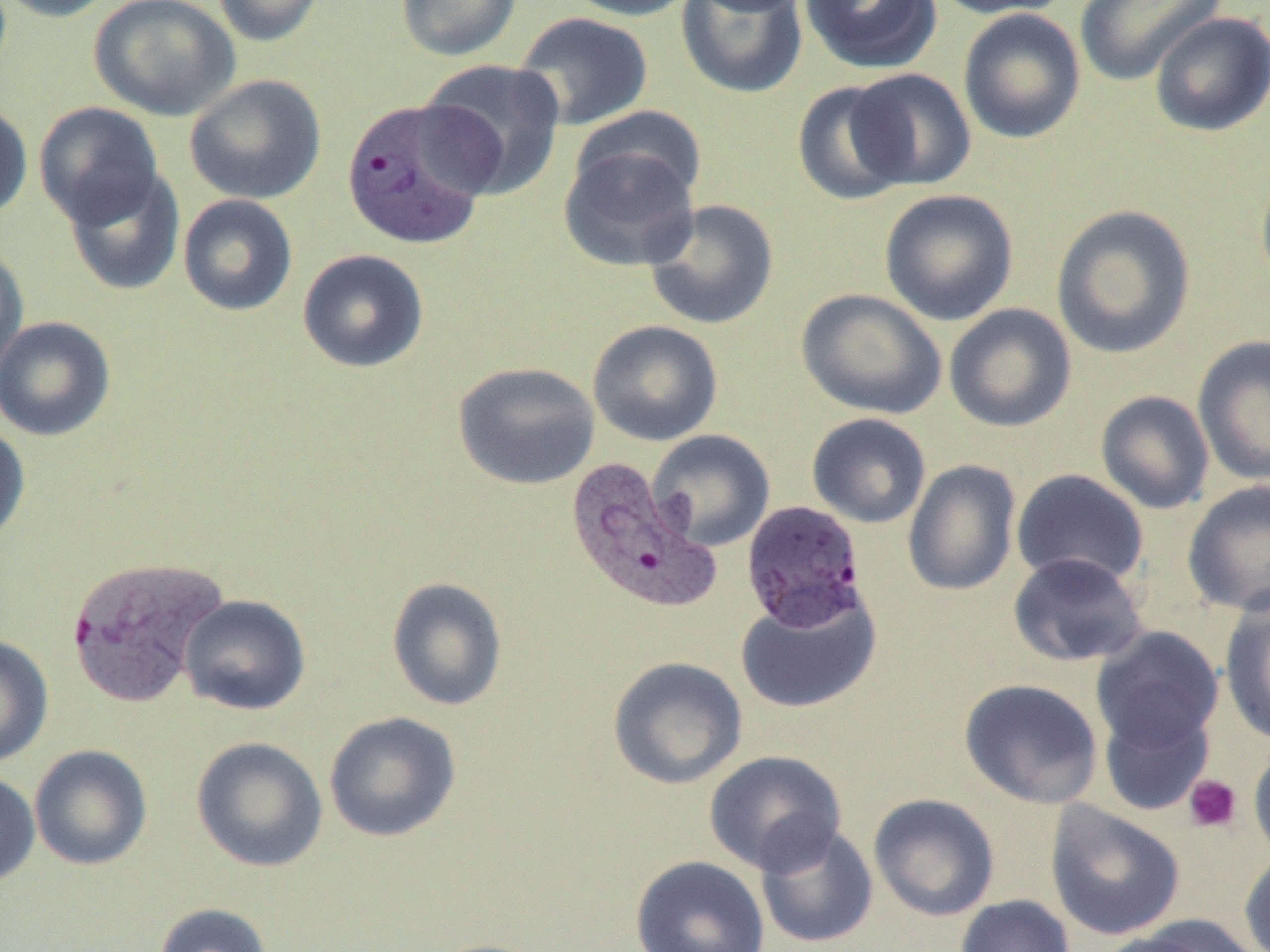
{
  "slide_level_diagnosis": "Plasmodium vivax",
  "modality": "optical microscopy",
  "magnification": "1000x",
  "field_of_view": "one of a larger specimen",
  "plasmodium_vivax_infected_red_blood_cell_locations": "approximate bounding boxes as named x1/y1/x2/y2 corners in pixels: (x1=340, y1=98, x2=496, y2=250), (x1=563, y1=458, x2=721, y2=615), (x1=741, y1=500, x2=867, y2=631), (x1=65, y1=554, x2=230, y2=707)",
  "preparation": "thin blood smear",
  "uninfected_red_blood_cell_locations": "approximate bounding boxes as named x1/y1/x2/y2 corners in pixels: (x1=0, y1=0, x2=119, y2=22), (x1=89, y1=0, x2=240, y2=121), (x1=212, y1=0, x2=326, y2=47), (x1=396, y1=0, x2=522, y2=61), (x1=560, y1=0, x2=699, y2=21), (x1=676, y1=0, x2=809, y2=99), (x1=686, y1=0, x2=812, y2=16), (x1=799, y1=0, x2=942, y2=74), (x1=928, y1=0, x2=1075, y2=20), (x1=1074, y1=0, x2=1228, y2=87), (x1=957, y1=8, x2=1086, y2=144), (x1=1149, y1=11, x2=1270, y2=137), (x1=513, y1=12, x2=653, y2=130), (x1=417, y1=59, x2=567, y2=199), (x1=846, y1=68, x2=976, y2=191), (x1=184, y1=74, x2=327, y2=205), (x1=791, y1=80, x2=915, y2=206), (x1=33, y1=101, x2=165, y2=228), (x1=0, y1=102, x2=33, y2=220), (x1=570, y1=106, x2=707, y2=207), (x1=558, y1=143, x2=702, y2=272), (x1=1255, y1=163, x2=1270, y2=294), (x1=63, y1=166, x2=186, y2=297), (x1=879, y1=189, x2=1019, y2=326), (x1=178, y1=194, x2=298, y2=316), (x1=643, y1=199, x2=779, y2=330), (x1=1050, y1=205, x2=1196, y2=359), (x1=0, y1=245, x2=29, y2=379), (x1=297, y1=248, x2=429, y2=373), (x1=796, y1=288, x2=947, y2=419), (x1=944, y1=304, x2=1077, y2=432), (x1=0, y1=316, x2=116, y2=441), (x1=587, y1=319, x2=724, y2=446), (x1=1192, y1=334, x2=1270, y2=487), (x1=452, y1=361, x2=601, y2=490), (x1=1095, y1=390, x2=1215, y2=514), (x1=806, y1=412, x2=931, y2=529), (x1=0, y1=421, x2=31, y2=548), (x1=647, y1=429, x2=776, y2=551), (x1=903, y1=459, x2=1022, y2=596), (x1=1011, y1=469, x2=1150, y2=588), (x1=1182, y1=480, x2=1270, y2=616), (x1=1007, y1=552, x2=1149, y2=667), (x1=386, y1=577, x2=508, y2=711), (x1=735, y1=584, x2=882, y2=715), (x1=178, y1=594, x2=311, y2=716), (x1=1219, y1=594, x2=1270, y2=746), (x1=1090, y1=626, x2=1224, y2=755), (x1=0, y1=635, x2=54, y2=766), (x1=607, y1=656, x2=748, y2=790), (x1=959, y1=678, x2=1104, y2=809), (x1=1098, y1=702, x2=1215, y2=816), (x1=323, y1=711, x2=462, y2=843), (x1=191, y1=736, x2=328, y2=871), (x1=1248, y1=738, x2=1270, y2=863), (x1=29, y1=744, x2=153, y2=870), (x1=703, y1=750, x2=847, y2=875), (x1=0, y1=771, x2=40, y2=887), (x1=868, y1=793, x2=1001, y2=922), (x1=1045, y1=801, x2=1185, y2=940), (x1=754, y1=821, x2=879, y2=949), (x1=1239, y1=848, x2=1270, y2=952), (x1=630, y1=855, x2=770, y2=952), (x1=954, y1=894, x2=1076, y2=952), (x1=154, y1=903, x2=274, y2=952), (x1=1113, y1=915, x2=1265, y2=952), (x1=1091, y1=928, x2=1226, y2=952), (x1=424, y1=937, x2=551, y2=952)",
  "platelet_locations": "approximate bounding boxes as named x1/y1/x2/y2 corners in pixels: (x1=1184, y1=774, x2=1242, y2=833)",
  "image_size": "1270×952 pixels"
}